Classify this cell by malaria status.
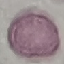
It is uninfected.

Summary:
  - Preparation: thin smear
  - Stain: Giemsa
  - Image type: automatically extracted cell patch, resized to 64 × 64 pixels
  - Capture: smartphone camera at the microscope eyepiece